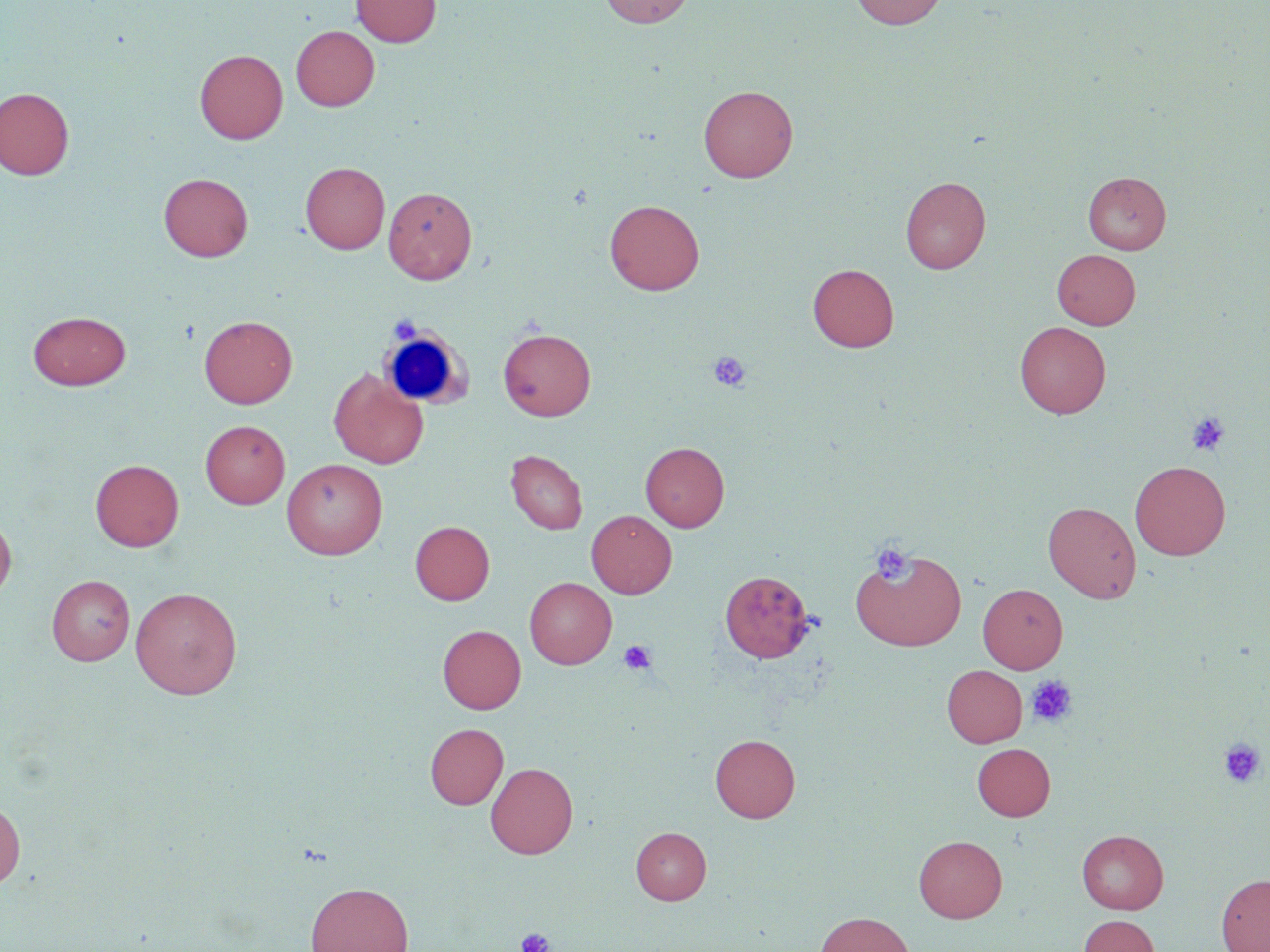

Summary:
  - Coordinate format: approximate bounding boxes as (x1, y1, x2, y2) in pixels
  - White blood cell locations: (377, 322, 480, 412)
  - Platelet locations: (388, 315, 422, 341), (709, 351, 750, 392), (1186, 411, 1230, 456), (871, 544, 912, 583), (618, 640, 656, 675), (1026, 675, 1077, 727), (1219, 738, 1265, 788), (517, 927, 554, 952)
  - Uninfected red blood cell locations: (351, 0, 441, 46), (599, 0, 696, 28), (849, 0, 948, 29), (291, 25, 379, 111), (195, 49, 287, 144), (699, 85, 798, 182), (0, 87, 74, 180), (300, 161, 390, 254), (1084, 172, 1171, 254), (158, 173, 253, 262), (900, 176, 990, 274), (384, 186, 477, 284), (605, 200, 704, 295), (1052, 249, 1140, 329), (808, 263, 899, 352), (28, 311, 130, 390), (200, 315, 297, 408), (1015, 321, 1111, 418), (498, 328, 596, 421), (329, 368, 428, 468), (200, 420, 290, 509), (641, 442, 730, 531), (506, 449, 587, 534), (90, 458, 184, 552), (282, 458, 388, 559), (1130, 460, 1230, 560), (1043, 501, 1141, 603), (586, 510, 677, 598), (0, 513, 16, 603), (410, 521, 494, 605), (850, 547, 967, 651), (720, 570, 812, 663), (47, 575, 135, 665), (525, 577, 616, 669), (977, 583, 1067, 673), (131, 587, 242, 699), (438, 624, 526, 714), (942, 665, 1027, 747), (424, 723, 508, 809), (710, 734, 800, 822), (972, 743, 1055, 820), (486, 762, 578, 859), (0, 798, 25, 888), (631, 827, 711, 904), (1077, 830, 1169, 914), (914, 835, 1007, 923), (1217, 874, 1270, 952), (305, 882, 413, 952), (814, 911, 915, 952), (1078, 915, 1160, 952)
  - Slide-level diagnosis: no evidence of blood parasites
  - Preparation: thin blood film
  - Image size: 1270×952 pixels
  - Modality: light microscopy
  - Stain: May-Grünwald-Giemsa
  - Field of view: single
  - Magnification: 1000x